Give the preparation type.
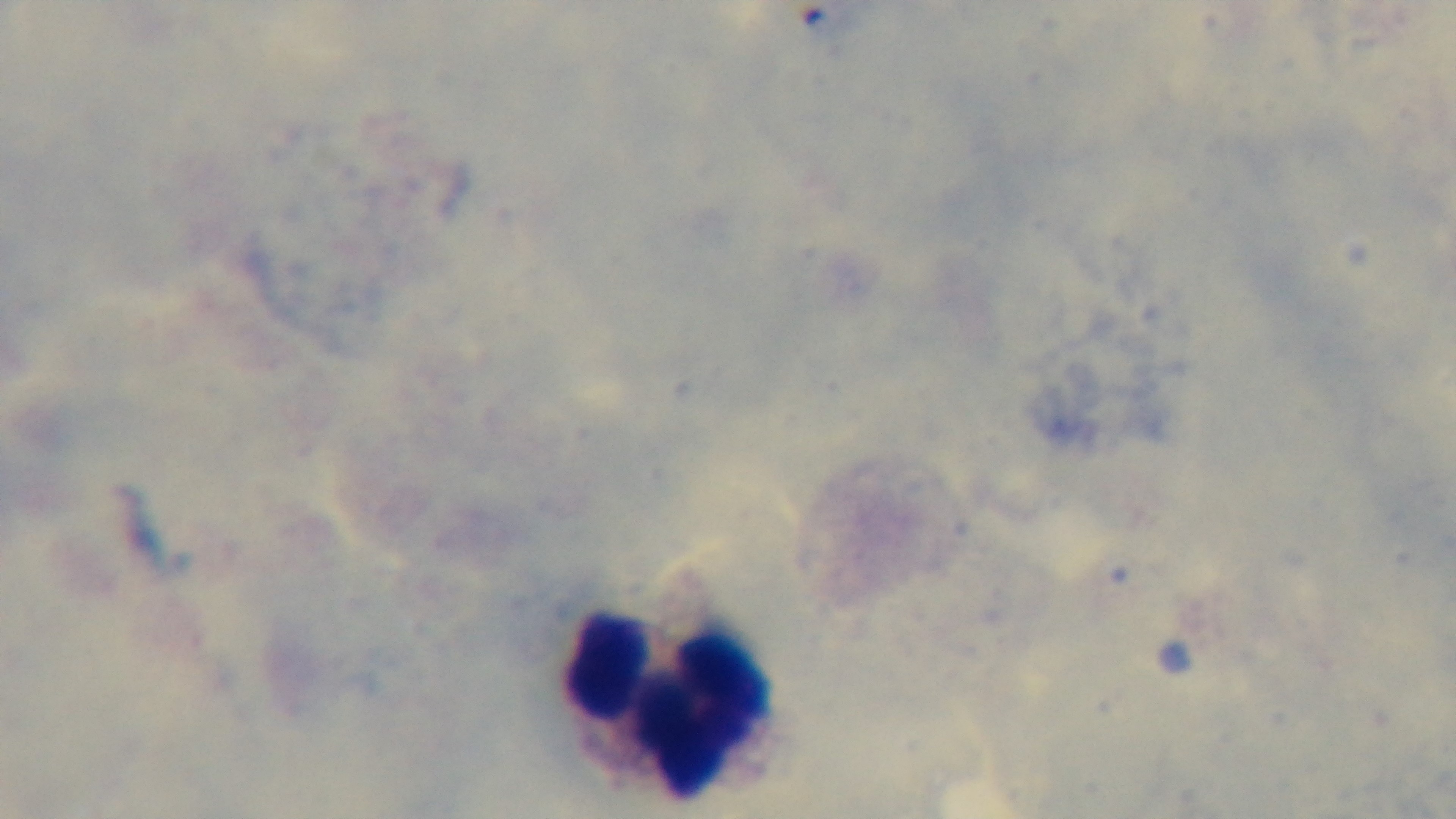

It is a thick blood film.

capture = mounted 4K digital camera
objective = 100x oil immersion
modality = light microscopy
field of view = one from the slide
stain = Giemsa
malaria status = uninfected